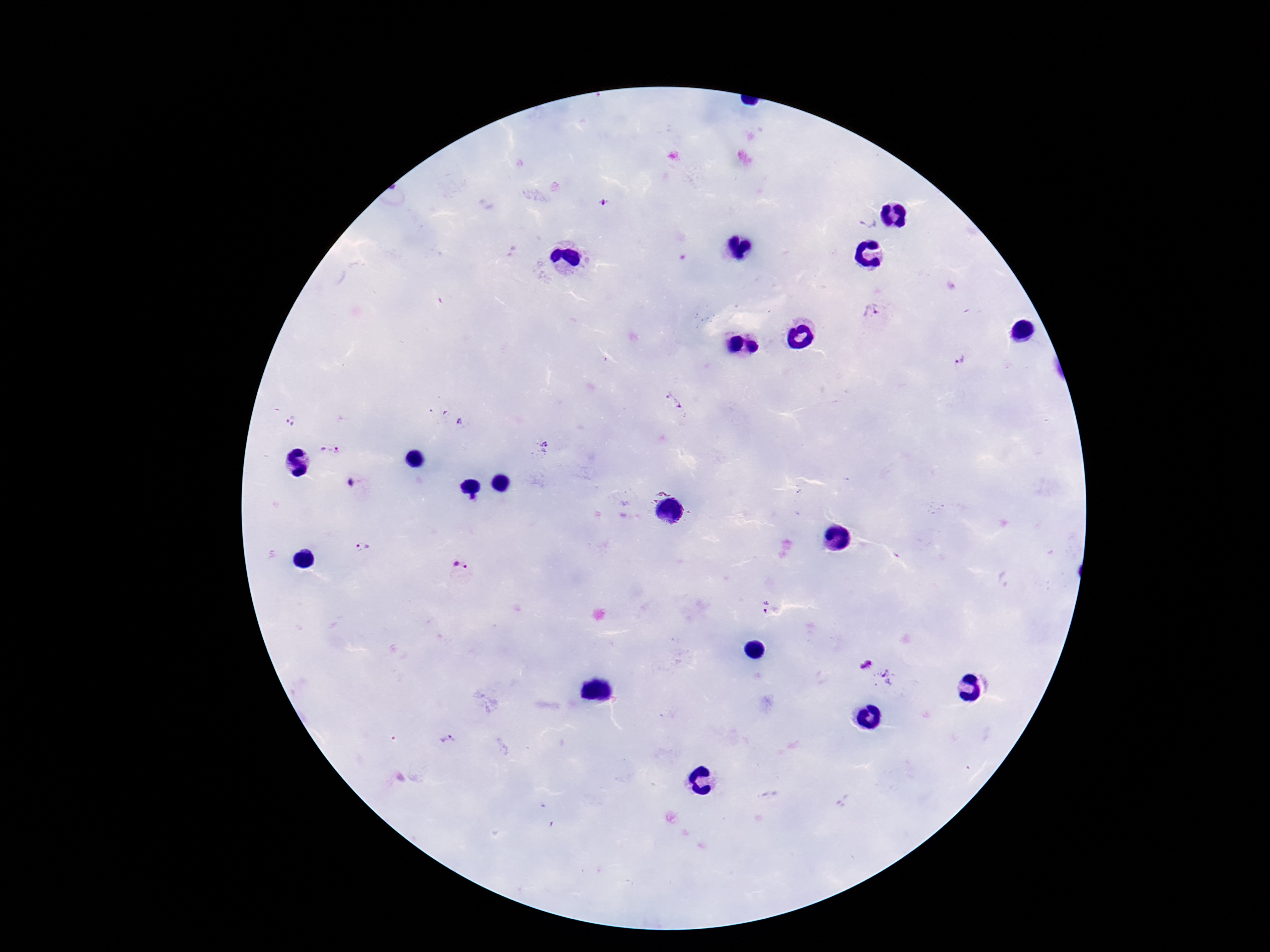 Approximate centers as (x, y) in pixels. Plasmodium parasite locations: (607, 202), (867, 223), (871, 312), (962, 357), (672, 402), (458, 421), (292, 422), (540, 449), (328, 451), (348, 483), (363, 547), (460, 568), (764, 607), (865, 664), (884, 677), (448, 740). Image is 1270×952 pixels. Patient malaria status: infected. One field from this slide. Giemsa-stained preparation. 100x magnification. Smartphone photograph taken through the microscope eyepiece. Thick blood film.